Classify this cell by malaria status.
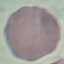

It is uninfected.

image type = cell patch, automatically extracted from a larger field of view and resized to 64 × 64 pixels
stain = Giemsa
preparation = thin smear
capture = smartphone through the microscope eyepiece